Locate every Plasmodium parasite.
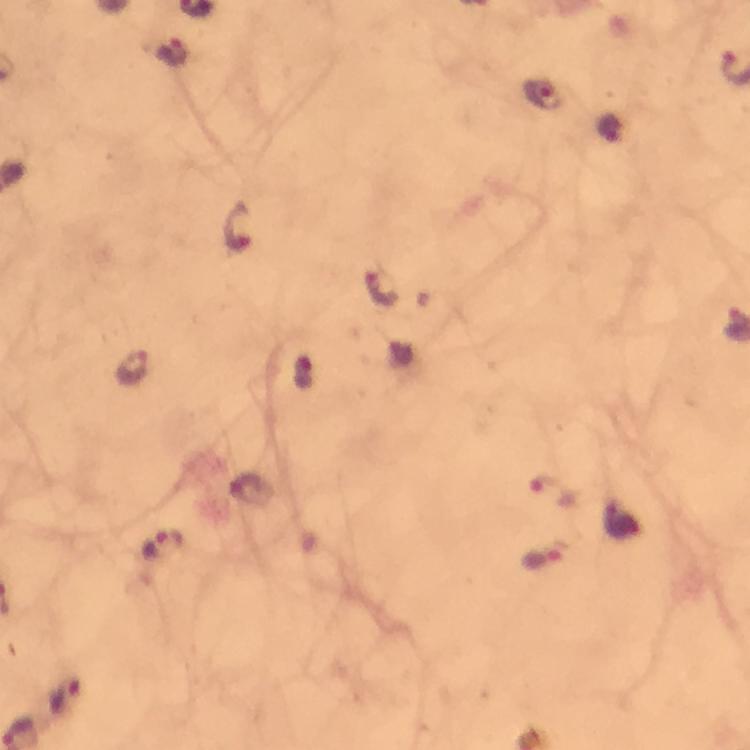

Approximate centers as [x, y] in pixels.
Plasmodium parasites: [173, 51], [543, 95], [237, 227], [380, 287], [132, 367], [554, 490], [164, 547], [544, 559], [64, 694].

Summary:
  - Cropped from: one field of view
  - Stain: Giemsa
  - Immersion oil: used
  - Context: from a malaria diagnostic workup
  - Image size: 750×750 pixels
  - Magnification: 100x
  - Capture: smartphone mounted on the microscope
  - Preparation: thick blood film